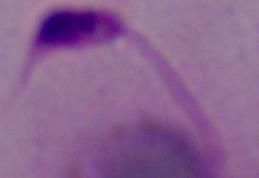
{
  "identification": "Leishmania",
  "magnification": "1000x",
  "modality": "micrograph"
}